Assess this cell for malaria.
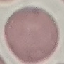
It is uninfected.

Giemsa-stained preparation. Cell patch, automatically extracted from a larger field of view and resized to 64 × 64 pixels. Thin blood smear. Photographed with a smartphone camera at the microscope eyepiece.